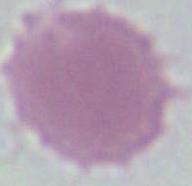
Summary:
  - Identification: erythrocyte
  - Magnification: 1000x
  - Modality: micrograph